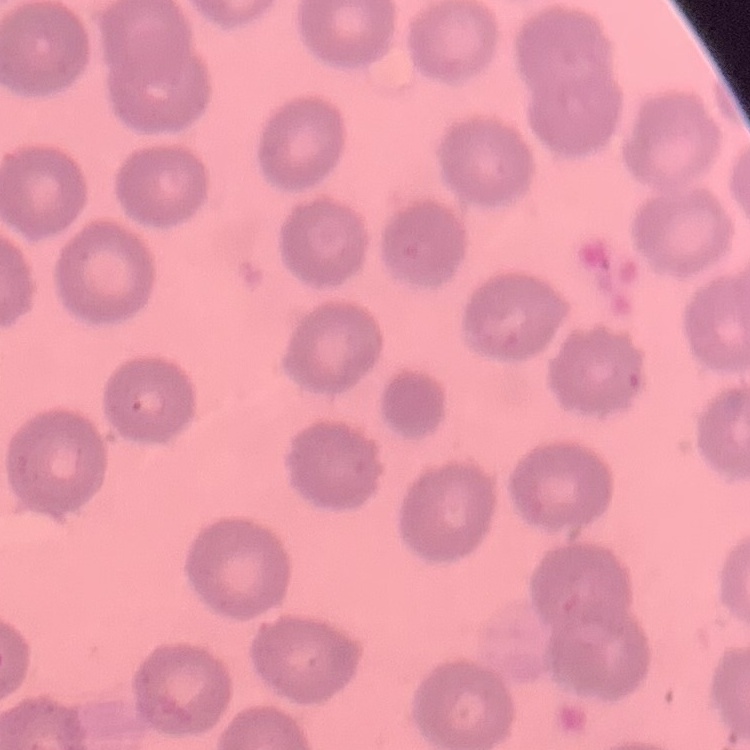

The red blood cells exhibit no rouleaux formation. Thin peripheral smear. Stained with either Field's or Giemsa. One tile cut from a larger photomicrograph.